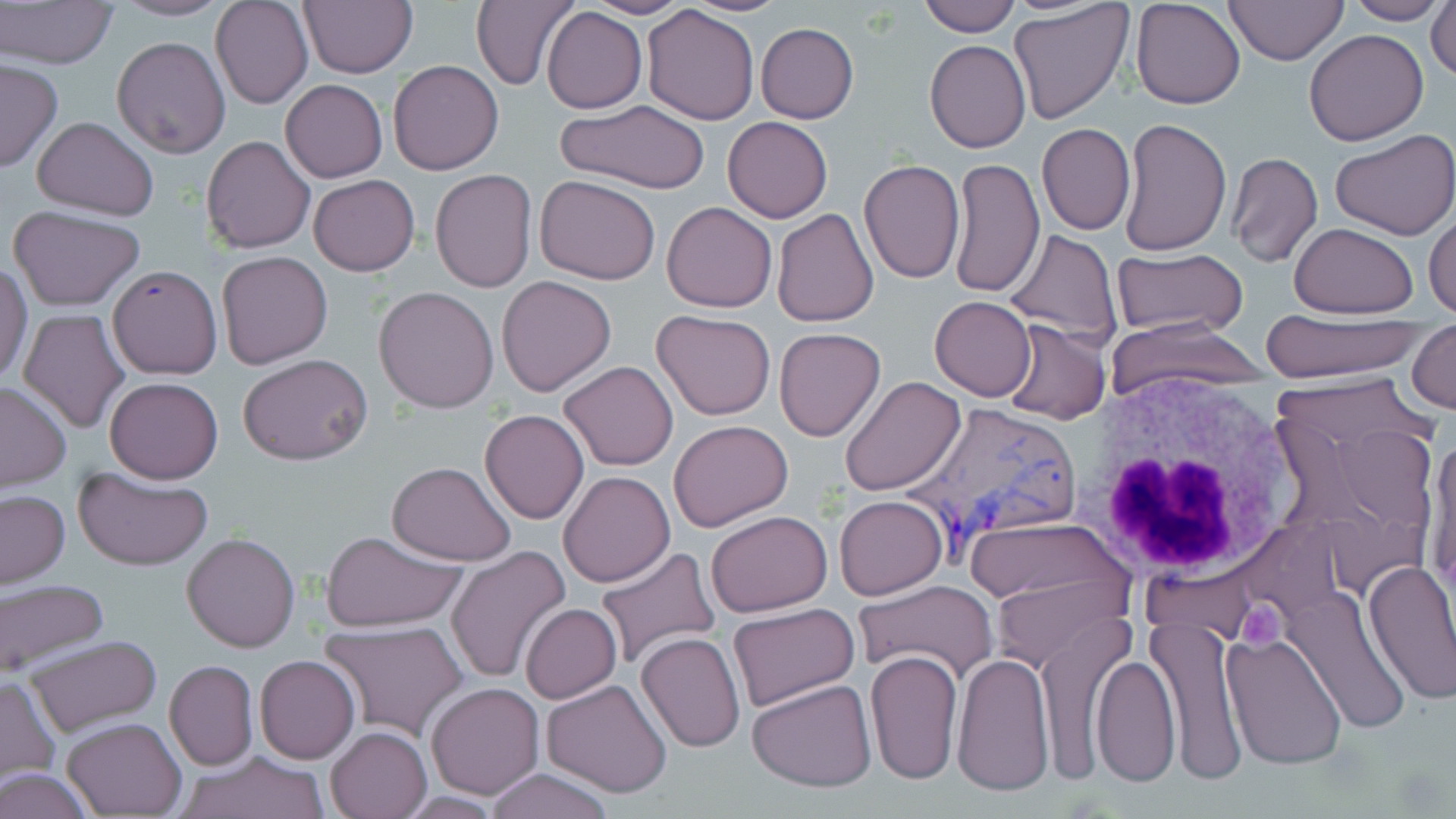
Summary:
  - Coordinate format: approximate bounding boxes as (x1, y1, x2, y2) in pixels
  - Uninfected red blood cell locations: (211, 0, 313, 109), (298, 0, 418, 78), (683, 0, 791, 16), (916, 0, 1020, 37), (1130, 0, 1246, 109), (1224, 0, 1348, 66), (1341, 0, 1450, 25), (1427, 0, 1456, 83), (1, 1, 120, 70), (111, 1, 234, 21), (470, 1, 577, 89), (581, 1, 695, 19), (1010, 2, 1135, 126), (642, 5, 760, 126), (541, 7, 646, 113), (755, 22, 858, 123), (1304, 28, 1430, 146), (112, 36, 232, 158), (926, 40, 1031, 154), (0, 58, 62, 172), (387, 60, 505, 175), (280, 79, 388, 183), (555, 100, 711, 195), (32, 116, 160, 220), (722, 116, 833, 223), (1118, 117, 1231, 256), (1038, 124, 1136, 235), (1331, 129, 1456, 241), (201, 135, 315, 253), (1227, 152, 1323, 268), (949, 157, 1045, 299), (859, 158, 966, 284), (428, 169, 538, 294), (307, 174, 420, 276), (536, 175, 659, 285), (662, 201, 777, 313), (9, 205, 146, 310), (772, 209, 877, 327), (1425, 210, 1456, 320), (1288, 222, 1420, 318), (1005, 229, 1122, 346), (1112, 248, 1247, 339), (216, 251, 334, 369), (0, 264, 33, 384), (108, 265, 223, 380), (495, 275, 618, 397), (373, 286, 500, 413), (930, 296, 1036, 401), (19, 308, 131, 434), (651, 309, 778, 422), (1260, 312, 1427, 382), (1106, 318, 1270, 396), (1002, 320, 1111, 424), (1409, 322, 1455, 414), (774, 328, 886, 441), (238, 354, 373, 465), (559, 360, 679, 471), (839, 375, 965, 497), (105, 376, 223, 484), (0, 381, 72, 490), (479, 409, 589, 525), (668, 419, 794, 533), (1422, 429, 1455, 603), (386, 462, 517, 566), (72, 466, 214, 571), (557, 471, 675, 588), (343, 480, 517, 615), (0, 490, 70, 590), (833, 496, 948, 601), (704, 509, 834, 618), (964, 513, 1136, 636), (317, 530, 468, 633), (182, 533, 300, 652), (593, 545, 721, 670), (446, 546, 571, 684), (1362, 559, 1456, 704), (0, 579, 109, 678), (854, 579, 998, 685), (1283, 586, 1413, 735), (519, 603, 622, 703), (727, 603, 859, 714), (1033, 614, 1128, 783), (1147, 615, 1248, 781), (320, 621, 469, 742), (635, 632, 746, 753), (1220, 633, 1348, 771), (23, 635, 163, 739), (865, 648, 964, 786), (952, 653, 1055, 798), (255, 655, 359, 763), (1091, 655, 1180, 788), (165, 660, 259, 771), (0, 676, 59, 783), (746, 678, 877, 790), (541, 679, 673, 797), (426, 683, 543, 798), (63, 717, 185, 818), (325, 726, 432, 818), (175, 749, 329, 819), (483, 767, 620, 819), (1, 768, 96, 819)
  - Platelet locations: (1234, 599, 1287, 645)
  - White blood cell locations: (1084, 376, 1311, 592)
  - Plasmodium vivax-infected red blood cell locations: (899, 401, 1086, 553)
  - Slide-level diagnosis: Plasmodium vivax
  - Field of view: single
  - Image size: 1456×819 pixels
  - Preparation: thin blood smear
  - Modality: light microscopy
  - Stain: May-Grünwald-Giemsa
  - Magnification: 1000x